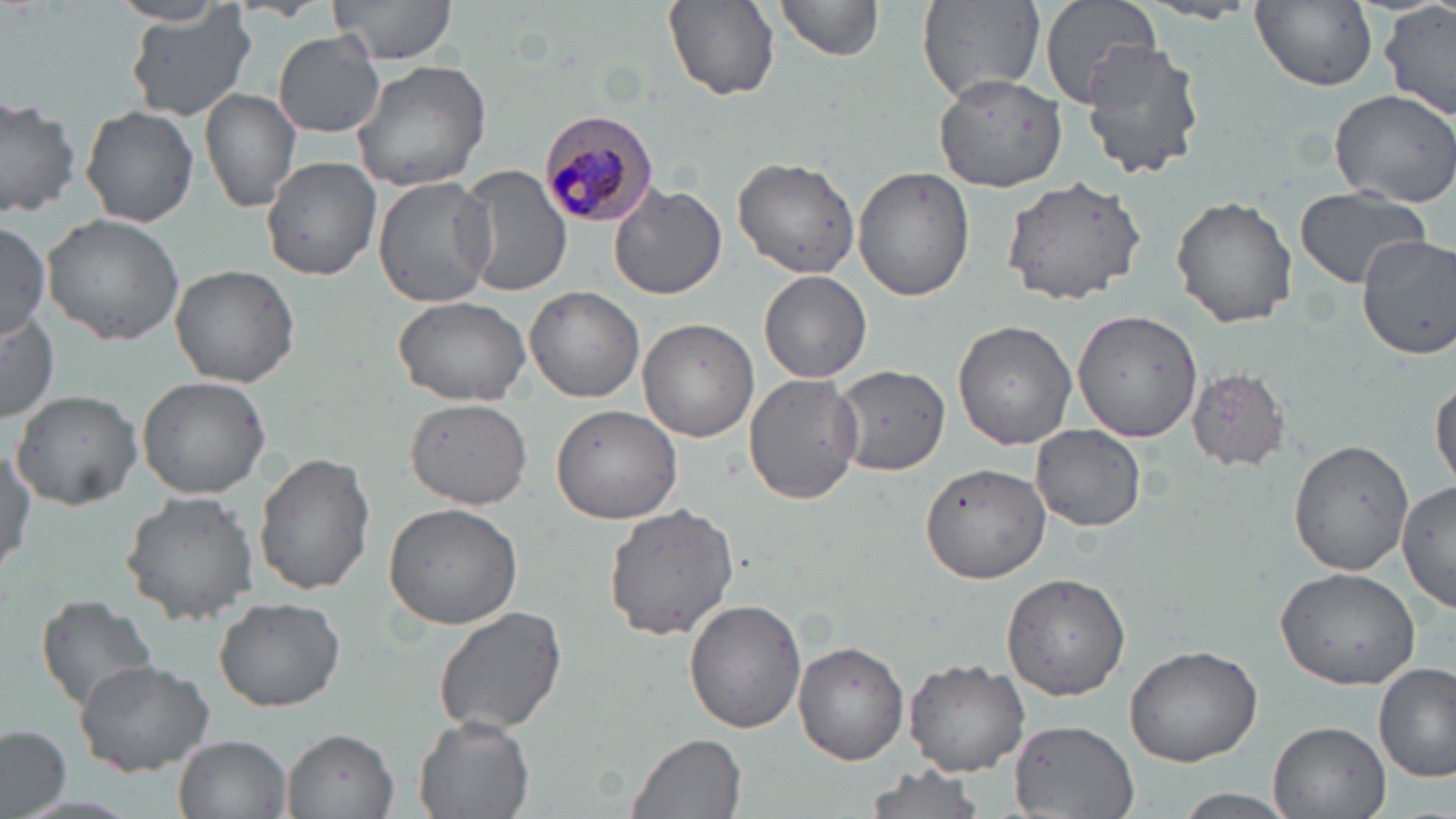

Summary:
  - Coordinate format: approximate bounding boxes as (x1,y1)-(x2,y2) corner pairs in pixels
  - Uninfected red blood cell locations: (329,0)-(459,66), (664,0)-(780,100), (917,0)-(1045,103), (1037,0)-(1161,108), (1251,0)-(1377,91), (775,1)-(883,65), (110,2)-(231,26), (1381,3)-(1455,122), (122,5)-(257,122), (273,33)-(386,139), (1080,41)-(1207,178), (353,58)-(496,192), (933,69)-(1070,191), (1327,87)-(1456,208), (200,89)-(301,214), (0,101)-(82,216), (81,107)-(199,227), (731,155)-(864,280), (261,156)-(381,280), (454,167)-(573,296), (853,167)-(975,302), (372,172)-(495,309), (1001,175)-(1148,306), (609,182)-(726,298), (1294,190)-(1431,291), (1171,196)-(1298,327), (42,212)-(188,346), (0,221)-(50,341), (1356,234)-(1456,358), (168,262)-(299,388), (758,270)-(873,383), (526,286)-(645,402), (391,294)-(531,405), (0,309)-(61,422), (1070,310)-(1204,442), (638,319)-(759,443), (952,320)-(1077,449), (834,364)-(946,477), (1187,368)-(1292,471), (743,373)-(864,505), (1431,373)-(1455,493), (136,375)-(272,499), (12,389)-(143,509), (405,397)-(533,510), (550,403)-(683,523), (1031,424)-(1147,531), (1287,436)-(1416,575), (1,441)-(35,583), (256,452)-(376,596), (918,461)-(1054,585), (1399,480)-(1456,614), (121,490)-(262,621), (383,501)-(523,631), (600,502)-(740,640), (1274,566)-(1424,690), (1000,569)-(1134,700), (35,593)-(160,716), (215,597)-(343,712), (685,600)-(805,732), (432,605)-(571,738), (795,643)-(908,765), (1123,644)-(1264,768), (903,657)-(1029,775), (74,659)-(214,774), (1375,662)-(1454,785), (414,714)-(534,819), (1010,719)-(1142,819), (1268,720)-(1392,819), (0,725)-(73,818), (283,730)-(398,817), (629,732)-(748,819), (175,735)-(291,818), (861,765)-(988,819), (1172,789)-(1297,819)
  - Plasmodium malariae-infected red blood cell locations: (540,107)-(663,228)
  - Slide-level diagnosis: Plasmodium malariae
  - Modality: optical microscopy
  - Stain: May-Grünwald-Giemsa
  - Preparation: thin blood film
  - Image size: 1456×819 pixels
  - Field of view: single
  - Magnification: 1000x